State which cell type is depicted.
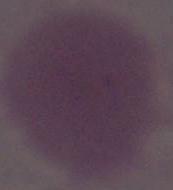
This is an erythrocyte.

Captured at 1000x magnification. Photomicrograph.